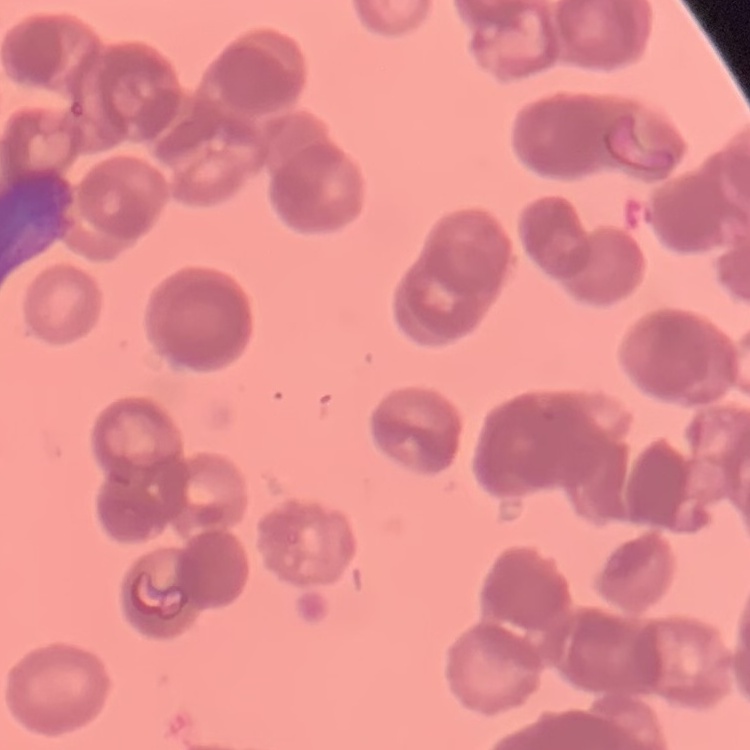
{
  "red_blood_cell_morphology": "rouleaux formation",
  "image_type": "square crop of a larger photomicrograph",
  "stain": "Field's or Giemsa",
  "preparation": "thin blood smear"
}